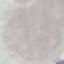 Result: negative for malaria parasites. Thin blood smear. Cell patch, automatically extracted from a larger field of view and resized to 64 × 64 pixels. Acquired by smartphone through the microscope eyepiece. Giemsa stain.